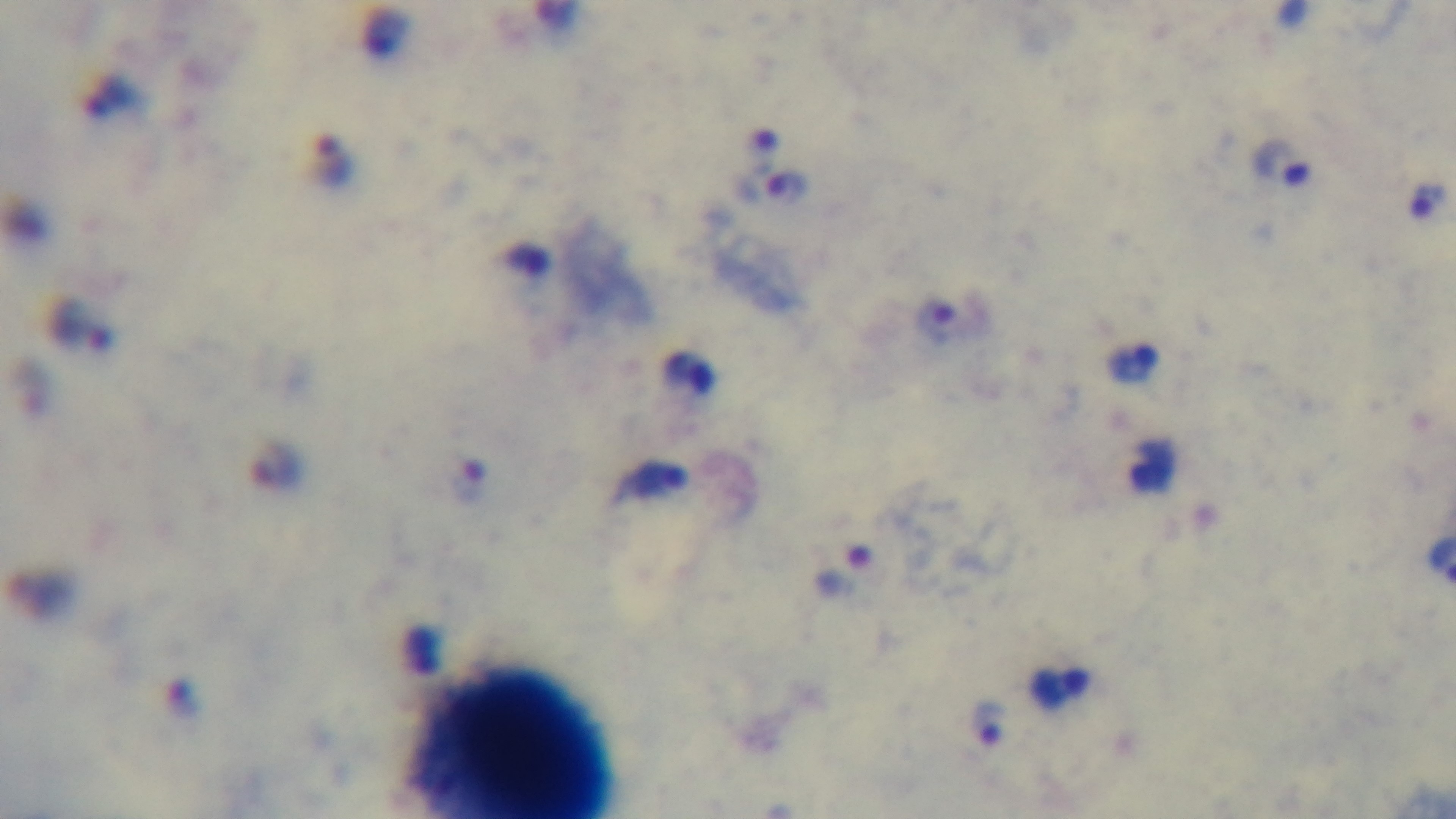
Preparation: thick smear. Captured with a mounted 4K digital camera. Light microscopy. Single field of view. Giemsa-stained. Malaria status: infected. 100x oil-immersion objective.